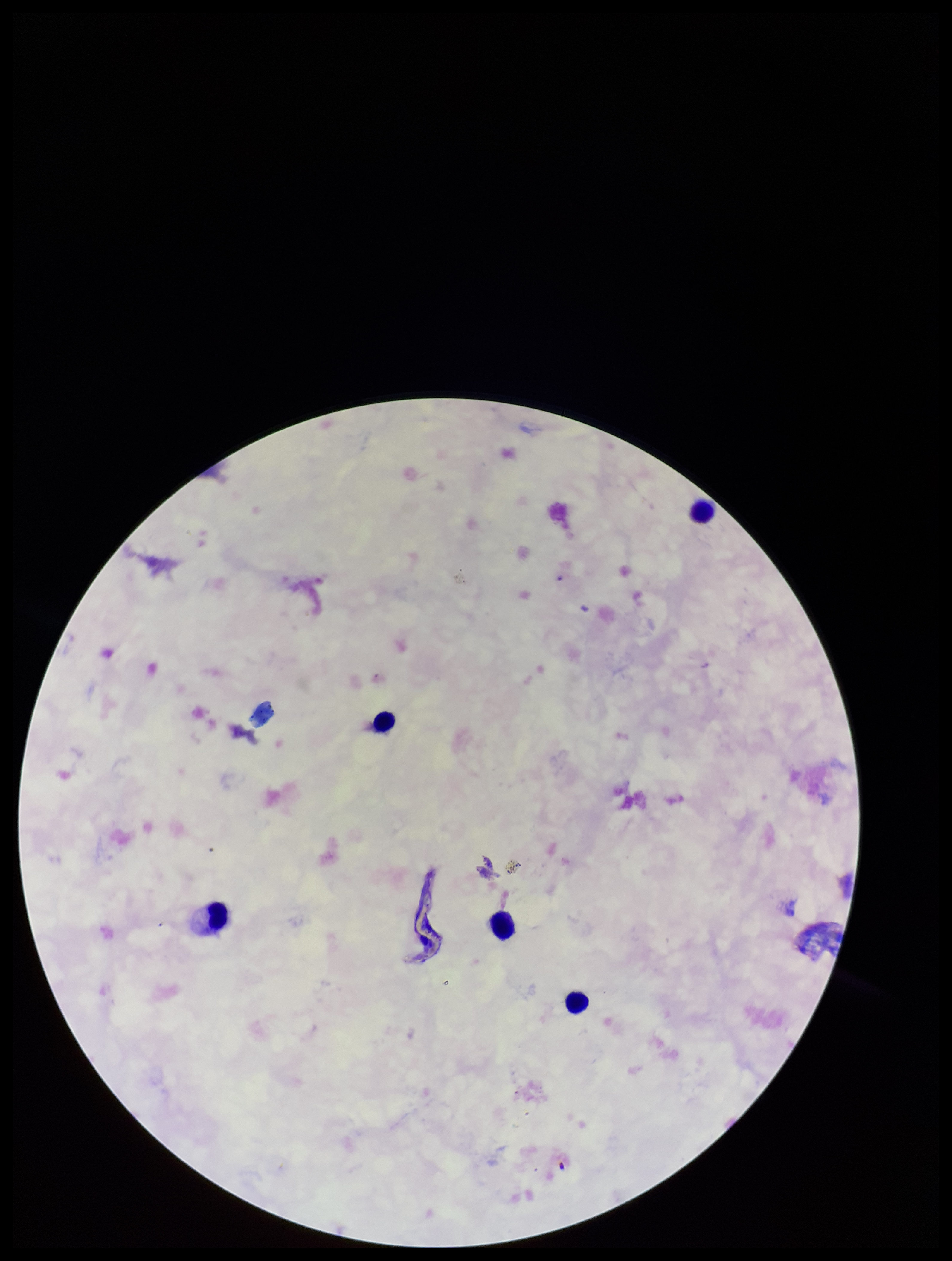

Preparation: thick blood smear. Image is 952×1261 pixels. Plasmodium parasites: none identified. One field from this slide. Smartphone photograph taken through the eyepiece of a microscope. Leukocyte count: 5. Parasite count: 0. Species reported for this patient: Plasmodium falciparum. Patient malaria status: infected. Giemsa stain.